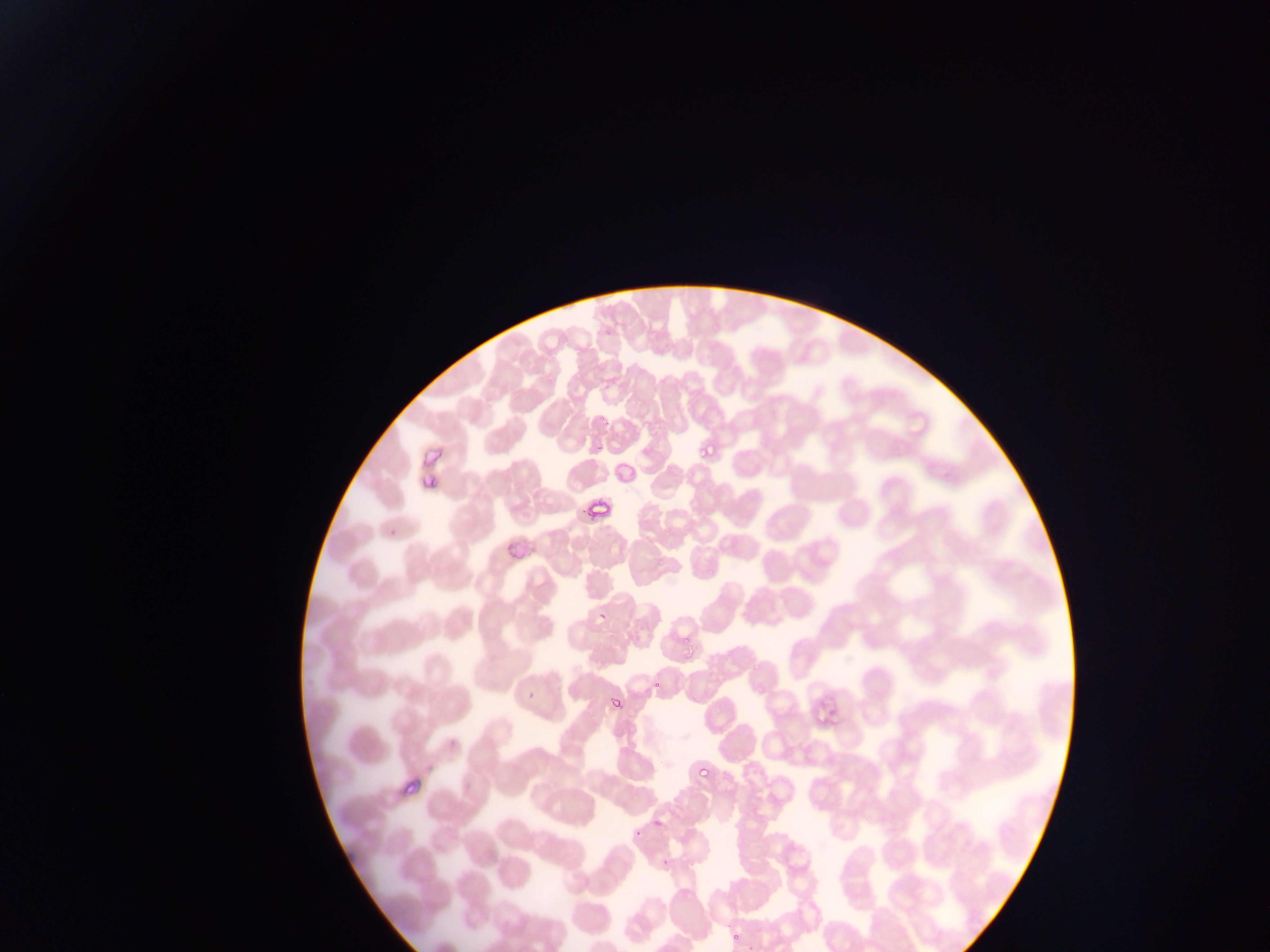
Approximate bounding boxes as (left, top, right, bottom) in pixels.
Summary:
  - Plasmodium parasite locations: (602, 325, 613, 338), (596, 413, 607, 424), (696, 442, 710, 464), (425, 475, 434, 487), (387, 515, 409, 537), (597, 608, 608, 622), (679, 637, 686, 650), (650, 677, 660, 693), (525, 690, 536, 702), (609, 694, 619, 717), (698, 759, 714, 780), (631, 827, 642, 841), (661, 856, 668, 867), (730, 931, 743, 942), (747, 944, 759, 951)
  - Capture: mobile-phone photograph through a microscope
  - Image size: 1270×952 pixels
  - Field of view: single
  - Preparation: thin blood smear
  - Country: Ghana